Identify the parasite.
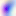

Toxoplasma gondii.

400x magnification. Photomicrograph.